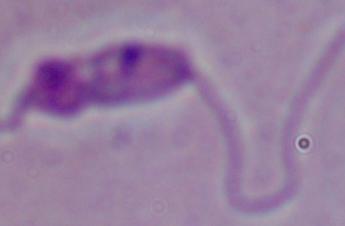
{
  "identification": "Leishmania",
  "magnification": "1000x",
  "modality": "micrograph"
}